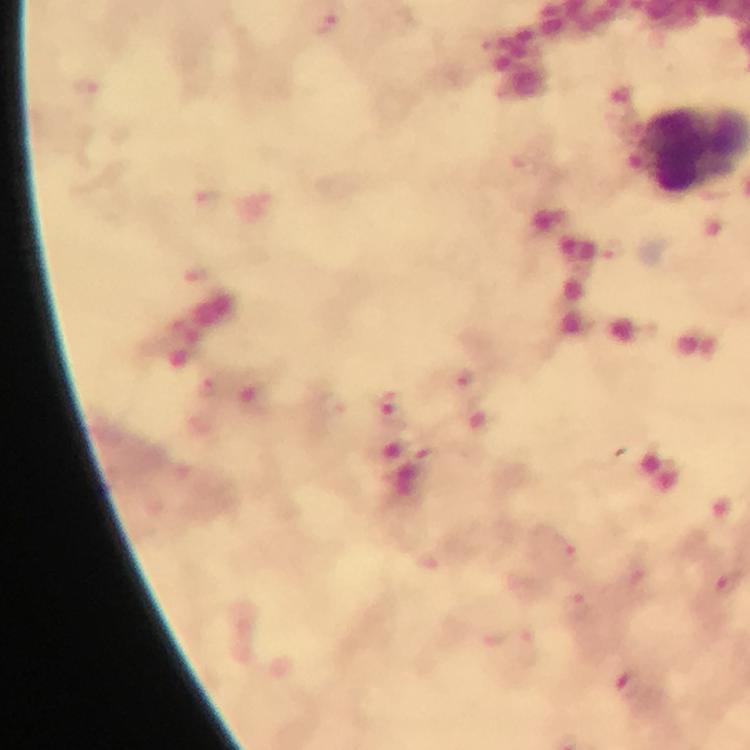
Approximate object centers, in pixels from the top-left corner. Malaria parasite locations: (x=327, y=22), (x=88, y=93), (x=209, y=202), (x=611, y=250), (x=198, y=278), (x=465, y=378), (x=209, y=387), (x=388, y=408), (x=567, y=552), (x=728, y=583). From a malaria diagnostic workup. Photographed with a smartphone mounted on the microscope. Thick blood smear. Cropped region of a single field of view. Giemsa stain. 100x magnification. Immersion oil applied. Image is 750×750 pixels.